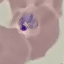

Summary:
  - Result: malaria parasites detected
  - Capture: smartphone camera at the microscope eyepiece
  - Image type: automatically extracted cell patch, resized to 64 × 64 pixels
  - Stain: Giemsa
  - Preparation: thin blood film